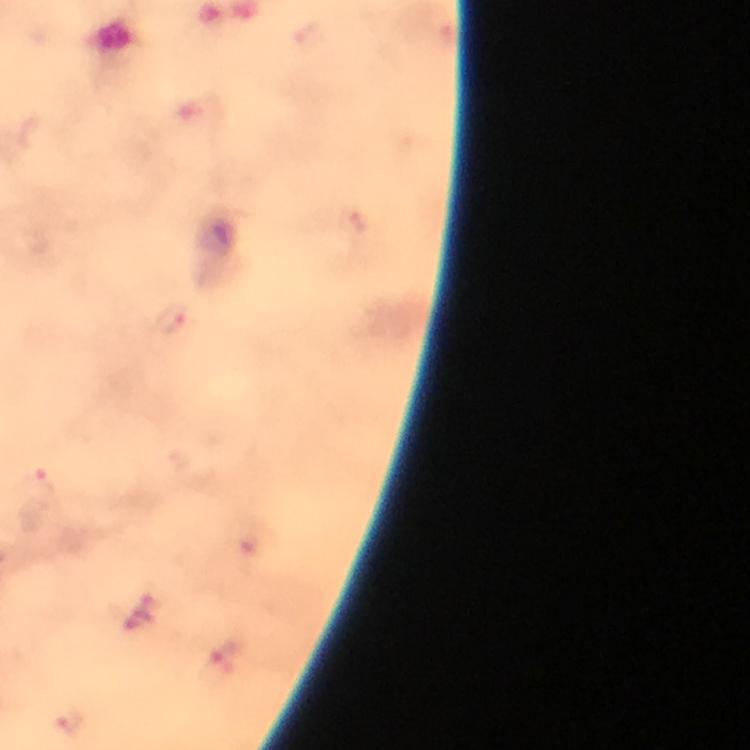
Approximate centers as {x, y} in pixels. Plasmodium parasite locations: {173, 319}, {40, 477}, {72, 722}. Immersion oil applied. From a diagnostic examination for malaria. Giemsa stain. At 100x magnification. Thick blood smear. Image is 750×750 pixels. A crop from one field of view. Smartphone photograph taken through a microscope.